State which cell type is depicted.
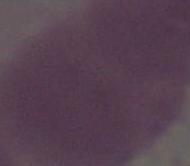

This is an erythrocyte.

Captured at 1000x magnification. Micrograph.